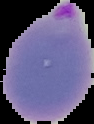
image type = cell region segmented out of the field of view; surrounding area masked to black
preparation = thin blood smear
image size = 94×124 pixels
malaria status = parasitized